Assess for malaria.
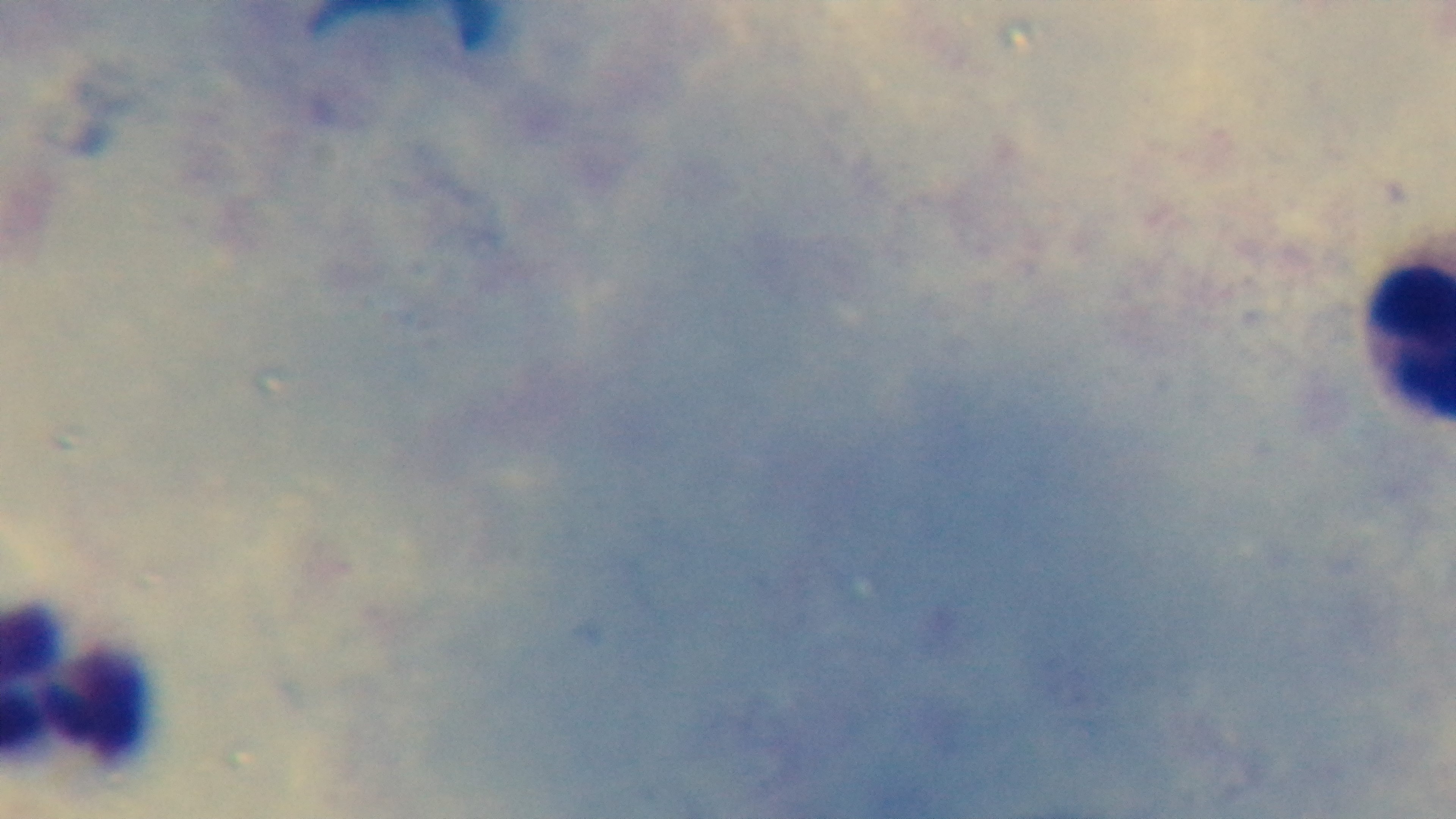

It is uninfected.

{
  "modality": "light microscopy",
  "field_of_view": "one from the slide",
  "capture": "mounted 4K digital camera",
  "stain": "Giemsa",
  "preparation": "thick smear",
  "objective": "100x oil immersion"
}